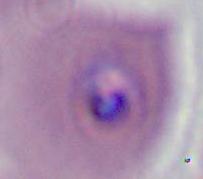

Summary:
  - Modality: photomicrograph
  - Identification: Plasmodium
  - Magnification: 400x or 1000x